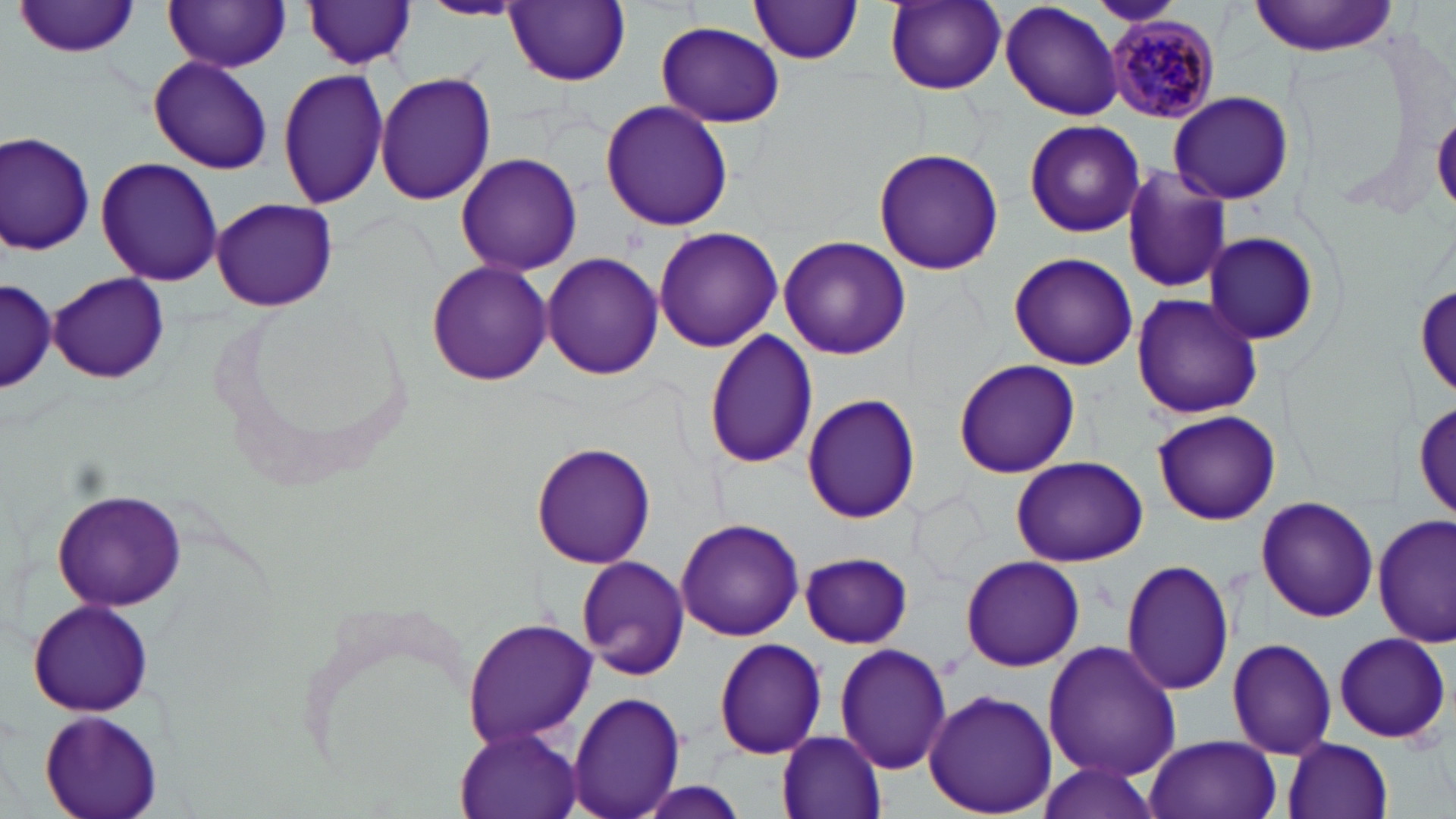
Summary:
  - Coordinate format: approximate bounding boxes as (x1, y1, x2, y2) in pixels
  - Plasmodium malariae-infected red blood cell locations: (1106, 15, 1221, 126)
  - Uninfected red blood cell locations: (1088, 0, 1181, 26), (1250, 0, 1398, 56), (16, 1, 144, 57), (163, 1, 292, 71), (417, 1, 528, 21), (748, 1, 866, 64), (883, 1, 1007, 95), (302, 2, 418, 70), (505, 2, 629, 87), (1000, 2, 1124, 121), (656, 20, 786, 127), (148, 55, 273, 174), (277, 66, 393, 211), (375, 71, 497, 206), (1168, 90, 1293, 205), (599, 99, 734, 232), (1433, 110, 1456, 215), (1021, 119, 1146, 238), (1, 131, 97, 255), (870, 146, 1005, 276), (454, 152, 584, 277), (95, 157, 224, 285), (1120, 165, 1233, 295), (210, 197, 338, 312), (652, 225, 783, 353), (1203, 232, 1322, 346), (777, 234, 912, 359), (542, 251, 663, 381), (1007, 251, 1138, 371), (426, 260, 553, 388), (48, 272, 168, 385), (0, 276, 57, 395), (1412, 278, 1456, 405), (1131, 291, 1263, 420), (701, 328, 819, 471), (952, 359, 1081, 479), (800, 392, 922, 524), (1412, 392, 1455, 527), (1152, 410, 1280, 525), (529, 443, 658, 569), (1011, 455, 1147, 566), (52, 489, 187, 611), (1255, 497, 1379, 623), (1373, 513, 1455, 649), (674, 517, 803, 642), (798, 551, 913, 647), (575, 554, 691, 682), (960, 555, 1084, 672), (1119, 559, 1235, 695), (26, 598, 155, 718), (462, 616, 596, 750), (1332, 632, 1451, 745), (713, 637, 828, 759), (1226, 637, 1338, 758), (1043, 640, 1181, 782), (833, 643, 953, 775), (922, 689, 1058, 815), (568, 691, 685, 819), (42, 709, 163, 817), (453, 724, 583, 819), (777, 730, 887, 818), (1143, 734, 1280, 819), (1283, 737, 1394, 819), (1035, 762, 1163, 819), (630, 780, 753, 819)
  - Slide-level diagnosis: Plasmodium malariae
  - Stain: May-Grünwald-Giemsa
  - Field of view: single
  - Magnification: 1000x
  - Preparation: thin blood smear
  - Image size: 1456×819 pixels
  - Modality: light microscopy